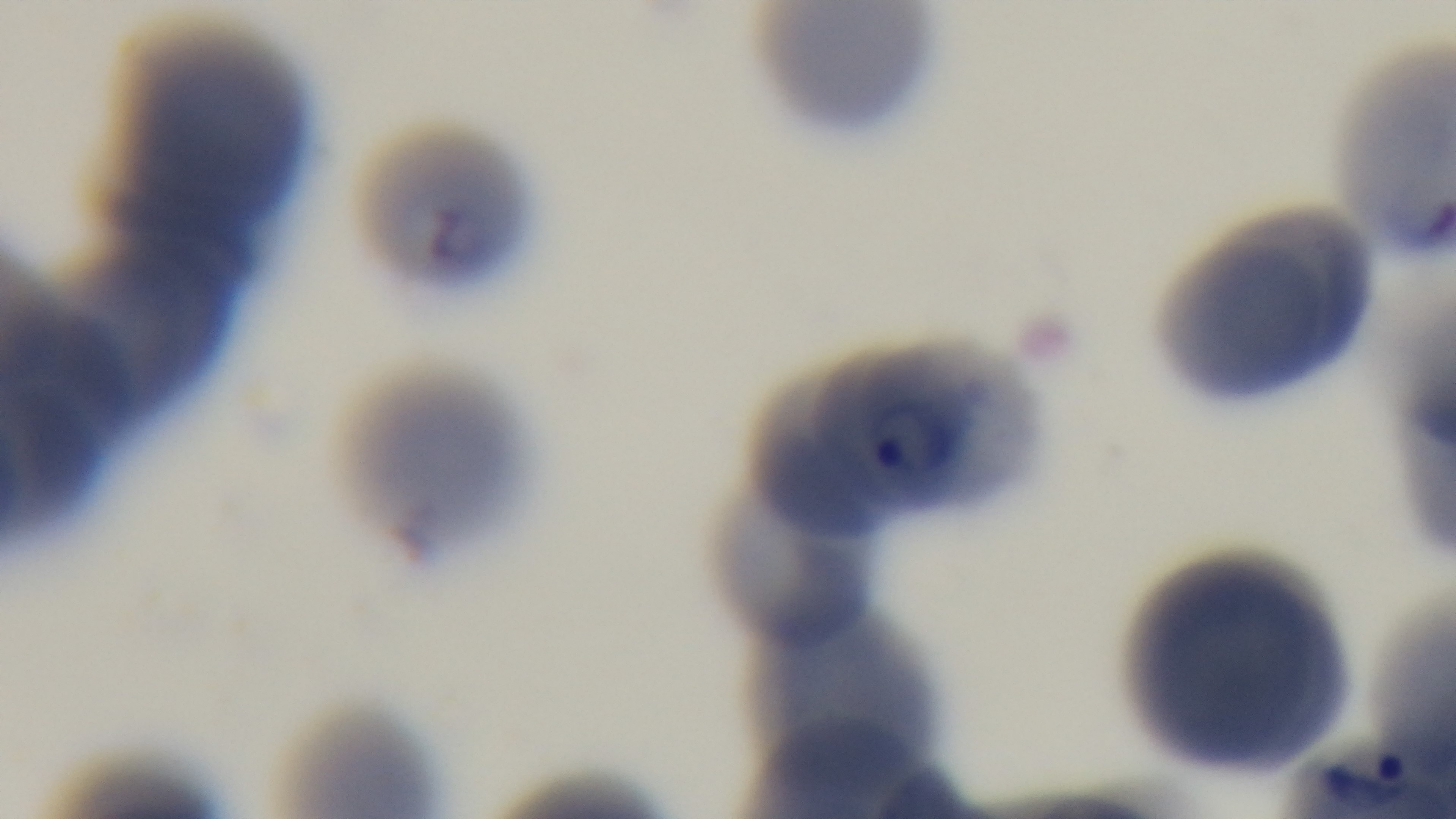
objective = 100x oil immersion
malaria status = positive
preparation = thin
modality = light microscopy
capture = mounted 4K digital camera
field of view = single
stain = Giemsa